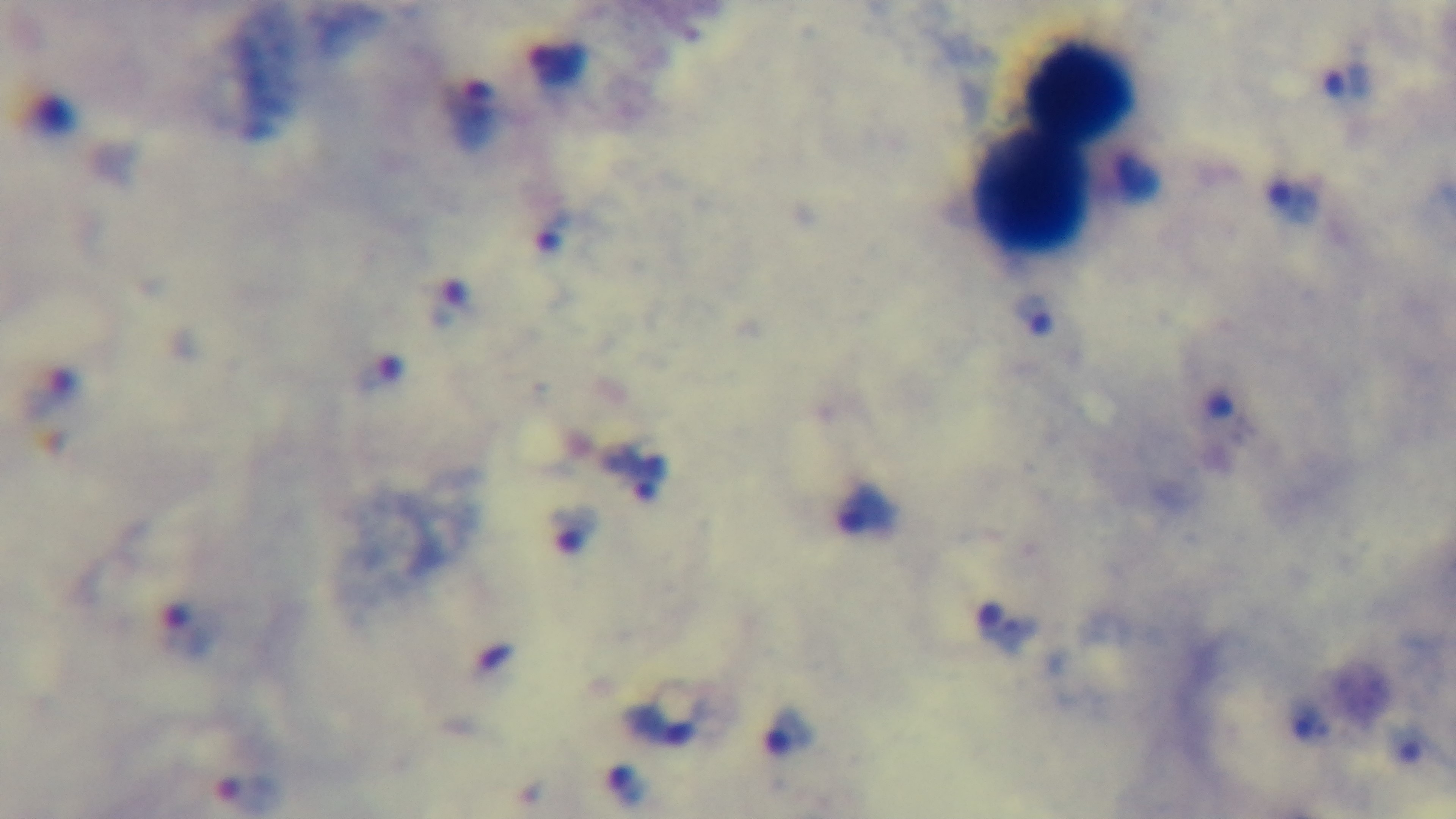

objective: 100x oil immersion
modality: light microscopy
capture: mounted 4K digital camera
preparation: thick blood film
malaria_status: positive
field_of_view: single
stain: Giemsa